Assess this cell for malaria.
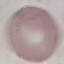
It is uninfected.

preparation = thin smear
capture = smartphone through the microscope eyepiece
image type = cell patch, automatically extracted from a larger field of view and resized to 64 × 64 pixels
stain = Giemsa